Comment on the morphology of the red blood cells.
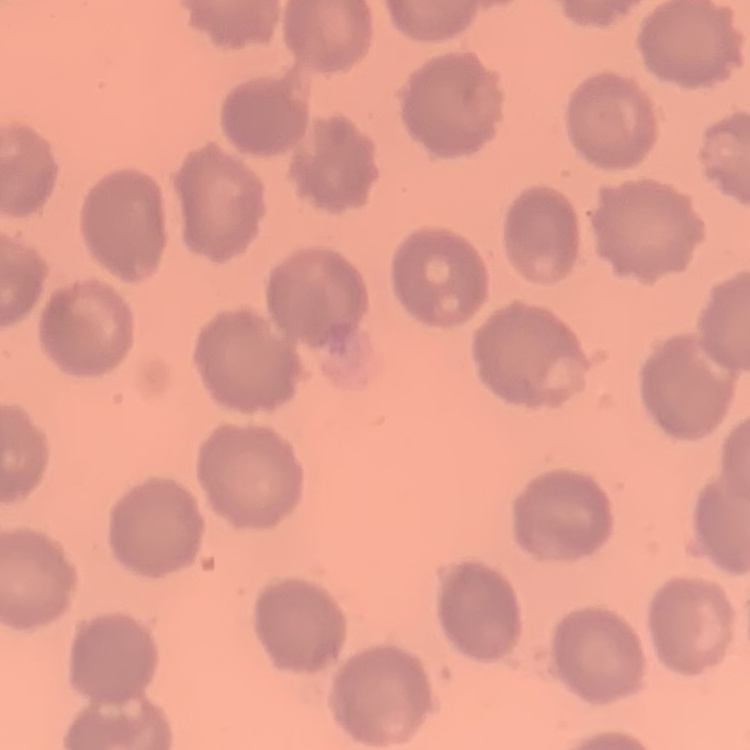
They show no rouleaux formation.

Summary:
  - Image type: one tile cut from a larger photomicrograph
  - Stain: Field's or Giemsa
  - Preparation: thin peripheral smear